Outline each Plasmodium falciparum-infected red blood cell.
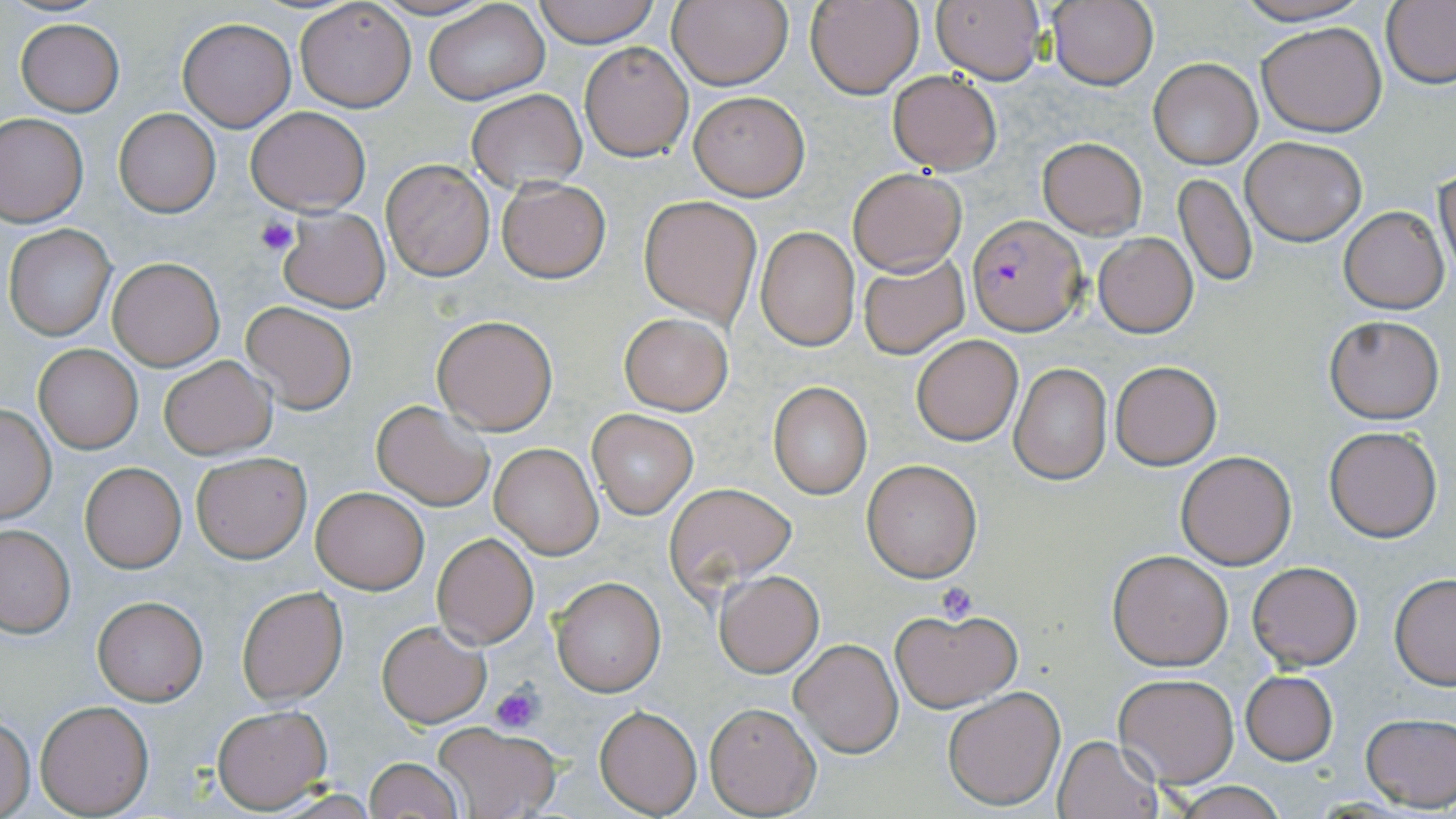

Approximate bounding boxes as named x1/y1/x2/y2 corners in pixels.
Plasmodium falciparum-infected red blood cells: (x1=966, y1=214, x2=1086, y2=336).

Summary:
  - Uninfected red blood cell locations: (x1=365, y1=0, x2=496, y2=21), (x1=532, y1=0, x2=661, y2=46), (x1=668, y1=0, x2=793, y2=91), (x1=806, y1=0, x2=923, y2=99), (x1=930, y1=0, x2=1048, y2=85), (x1=1047, y1=0, x2=1159, y2=91), (x1=1227, y1=0, x2=1376, y2=26), (x1=293, y1=1, x2=417, y2=112), (x1=1382, y1=2, x2=1456, y2=88), (x1=424, y1=3, x2=548, y2=105), (x1=15, y1=19, x2=124, y2=116), (x1=176, y1=19, x2=297, y2=131), (x1=1256, y1=22, x2=1386, y2=135), (x1=580, y1=42, x2=693, y2=161), (x1=1148, y1=59, x2=1262, y2=169), (x1=887, y1=71, x2=1002, y2=173), (x1=467, y1=89, x2=586, y2=191), (x1=688, y1=91, x2=810, y2=200), (x1=246, y1=106, x2=371, y2=214), (x1=113, y1=109, x2=220, y2=217), (x1=0, y1=113, x2=88, y2=226), (x1=1241, y1=135, x2=1366, y2=245), (x1=1037, y1=137, x2=1147, y2=239), (x1=381, y1=160, x2=494, y2=280), (x1=1436, y1=167, x2=1456, y2=284), (x1=846, y1=168, x2=966, y2=276), (x1=1174, y1=172, x2=1257, y2=288), (x1=496, y1=177, x2=610, y2=283), (x1=639, y1=195, x2=761, y2=326), (x1=1339, y1=207, x2=1449, y2=313), (x1=279, y1=208, x2=389, y2=312), (x1=5, y1=225, x2=114, y2=339), (x1=756, y1=227, x2=858, y2=350), (x1=1094, y1=232, x2=1198, y2=337), (x1=857, y1=252, x2=969, y2=358), (x1=107, y1=256, x2=225, y2=371), (x1=240, y1=301, x2=358, y2=415), (x1=619, y1=313, x2=733, y2=415), (x1=432, y1=315, x2=557, y2=434), (x1=1324, y1=316, x2=1444, y2=422), (x1=912, y1=334, x2=1023, y2=445), (x1=34, y1=344, x2=142, y2=453), (x1=158, y1=355, x2=276, y2=459), (x1=1111, y1=360, x2=1222, y2=470), (x1=1009, y1=363, x2=1112, y2=484), (x1=768, y1=382, x2=873, y2=498), (x1=371, y1=400, x2=494, y2=511), (x1=0, y1=404, x2=56, y2=522), (x1=589, y1=410, x2=696, y2=519), (x1=1324, y1=425, x2=1441, y2=541), (x1=490, y1=444, x2=602, y2=558), (x1=1175, y1=451, x2=1296, y2=570), (x1=192, y1=452, x2=312, y2=563), (x1=861, y1=459, x2=982, y2=582), (x1=80, y1=463, x2=186, y2=572), (x1=665, y1=482, x2=796, y2=594), (x1=312, y1=487, x2=428, y2=594), (x1=0, y1=525, x2=74, y2=636), (x1=432, y1=532, x2=538, y2=648), (x1=1108, y1=550, x2=1233, y2=670), (x1=1247, y1=561, x2=1362, y2=671), (x1=715, y1=570, x2=823, y2=676), (x1=1389, y1=574, x2=1456, y2=688), (x1=550, y1=575, x2=666, y2=697), (x1=237, y1=585, x2=348, y2=706), (x1=93, y1=596, x2=206, y2=705), (x1=888, y1=606, x2=1022, y2=711), (x1=375, y1=620, x2=491, y2=728), (x1=789, y1=639, x2=903, y2=757), (x1=1240, y1=670, x2=1338, y2=764), (x1=1113, y1=674, x2=1238, y2=787), (x1=942, y1=687, x2=1067, y2=810), (x1=36, y1=700, x2=153, y2=816), (x1=705, y1=703, x2=821, y2=817), (x1=213, y1=705, x2=332, y2=812), (x1=595, y1=705, x2=702, y2=816), (x1=1360, y1=712, x2=1456, y2=811), (x1=0, y1=715, x2=35, y2=817), (x1=433, y1=723, x2=561, y2=819), (x1=1053, y1=735, x2=1163, y2=819), (x1=364, y1=756, x2=462, y2=819), (x1=1167, y1=782, x2=1289, y2=819)
  - Platelet locations: (x1=255, y1=216, x2=300, y2=257), (x1=936, y1=582, x2=980, y2=623), (x1=490, y1=681, x2=545, y2=734)
  - Slide-level diagnosis: Plasmodium falciparum
  - Preparation: thin blood film
  - Image size: 1456×819 pixels
  - Modality: light microscopy
  - Stain: May-Grünwald-Giemsa
  - Magnification: 1000x
  - Field of view: single